Locate and identify every blood parasite.
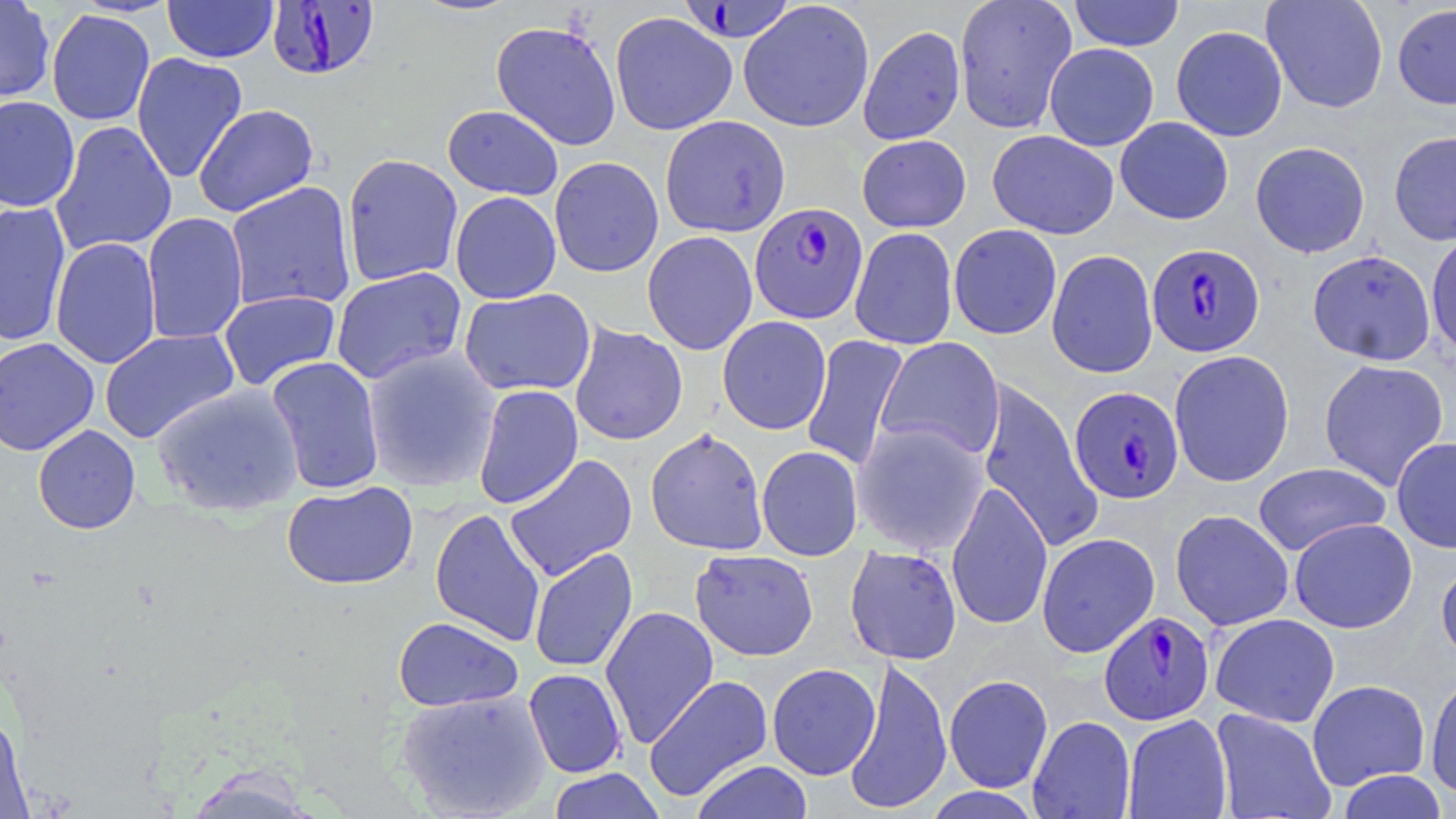

Approximate bounding boxes as named x1/y1/x2/y2 corners in pixels.
Plasmodium falciparum-infected red blood cells: (x1=681, y1=0, x2=792, y2=46), (x1=266, y1=1, x2=380, y2=80), (x1=749, y1=202, x2=868, y2=324), (x1=1147, y1=242, x2=1265, y2=357), (x1=1068, y1=385, x2=1184, y2=504), (x1=1099, y1=611, x2=1214, y2=725).
No Plasmodium ovale, Plasmodium malariae, Plasmodium vivax, Babesia divergens, or Trypanosoma brucei observed.

slide-level diagnosis = Plasmodium falciparum
field of view = one of a larger specimen
stain = May-Grünwald-Giemsa
image size = 1456×819 pixels
modality = optical microscopy
magnification = 1000x
uninfected red blood cell locations = approximate bounding boxes as named x1/y1/x2/y2 corners in pixels: (x1=0, y1=0, x2=56, y2=104), (x1=163, y1=0, x2=279, y2=63), (x1=409, y1=0, x2=523, y2=17), (x1=738, y1=0, x2=875, y2=133), (x1=953, y1=0, x2=1077, y2=134), (x1=1068, y1=0, x2=1184, y2=51), (x1=1261, y1=0, x2=1388, y2=113), (x1=1392, y1=3, x2=1456, y2=109), (x1=46, y1=8, x2=156, y2=126), (x1=610, y1=11, x2=737, y2=136), (x1=491, y1=20, x2=621, y2=150), (x1=858, y1=25, x2=966, y2=145), (x1=1171, y1=25, x2=1288, y2=141), (x1=1044, y1=43, x2=1159, y2=151), (x1=131, y1=52, x2=248, y2=183), (x1=0, y1=95, x2=81, y2=212), (x1=193, y1=104, x2=319, y2=217), (x1=442, y1=105, x2=564, y2=200), (x1=660, y1=115, x2=790, y2=237), (x1=652, y1=116, x2=771, y2=355), (x1=1115, y1=117, x2=1234, y2=225), (x1=50, y1=120, x2=177, y2=257), (x1=987, y1=130, x2=1119, y2=239), (x1=1389, y1=131, x2=1456, y2=245), (x1=857, y1=134, x2=971, y2=232), (x1=1250, y1=141, x2=1370, y2=258), (x1=341, y1=153, x2=464, y2=287), (x1=549, y1=156, x2=664, y2=278), (x1=224, y1=181, x2=357, y2=312), (x1=450, y1=191, x2=562, y2=304), (x1=0, y1=201, x2=72, y2=347), (x1=141, y1=212, x2=249, y2=345), (x1=948, y1=224, x2=1062, y2=340), (x1=849, y1=228, x2=958, y2=350), (x1=1426, y1=230, x2=1456, y2=358), (x1=642, y1=231, x2=758, y2=355), (x1=50, y1=237, x2=162, y2=369), (x1=1046, y1=249, x2=1158, y2=378), (x1=1307, y1=249, x2=1436, y2=365), (x1=331, y1=267, x2=467, y2=385), (x1=458, y1=288, x2=596, y2=396), (x1=217, y1=289, x2=342, y2=391), (x1=717, y1=316, x2=832, y2=435), (x1=569, y1=323, x2=688, y2=445), (x1=99, y1=328, x2=240, y2=443), (x1=801, y1=335, x2=909, y2=471), (x1=875, y1=336, x2=1005, y2=462), (x1=0, y1=337, x2=100, y2=456), (x1=362, y1=347, x2=501, y2=492), (x1=1169, y1=349, x2=1295, y2=487), (x1=265, y1=357, x2=386, y2=495), (x1=1318, y1=358, x2=1449, y2=491), (x1=976, y1=378, x2=1103, y2=554), (x1=150, y1=382, x2=305, y2=517), (x1=472, y1=384, x2=584, y2=509), (x1=852, y1=420, x2=989, y2=556), (x1=33, y1=425, x2=141, y2=534), (x1=645, y1=427, x2=769, y2=556), (x1=1391, y1=436, x2=1456, y2=553), (x1=756, y1=445, x2=863, y2=561), (x1=504, y1=454, x2=638, y2=582), (x1=1252, y1=462, x2=1390, y2=556), (x1=946, y1=480, x2=1053, y2=631), (x1=281, y1=481, x2=418, y2=589), (x1=430, y1=507, x2=546, y2=647), (x1=1170, y1=509, x2=1294, y2=630), (x1=1289, y1=518, x2=1417, y2=633), (x1=1036, y1=532, x2=1160, y2=658), (x1=845, y1=545, x2=962, y2=664), (x1=529, y1=547, x2=638, y2=673), (x1=690, y1=549, x2=819, y2=661), (x1=1436, y1=556, x2=1456, y2=668), (x1=599, y1=605, x2=719, y2=748), (x1=1210, y1=613, x2=1340, y2=727), (x1=393, y1=616, x2=523, y2=711), (x1=842, y1=656, x2=953, y2=814), (x1=767, y1=663, x2=880, y2=780), (x1=523, y1=668, x2=627, y2=778), (x1=1425, y1=672, x2=1456, y2=799), (x1=643, y1=674, x2=773, y2=802), (x1=944, y1=674, x2=1053, y2=793), (x1=1306, y1=679, x2=1430, y2=790), (x1=396, y1=688, x2=552, y2=817), (x1=1211, y1=708, x2=1336, y2=819), (x1=0, y1=710, x2=33, y2=819), (x1=1122, y1=714, x2=1233, y2=818), (x1=1028, y1=715, x2=1135, y2=819), (x1=690, y1=759, x2=814, y2=819), (x1=546, y1=768, x2=666, y2=819), (x1=1337, y1=770, x2=1448, y2=818), (x1=921, y1=787, x2=1044, y2=819)
preparation = thin blood film